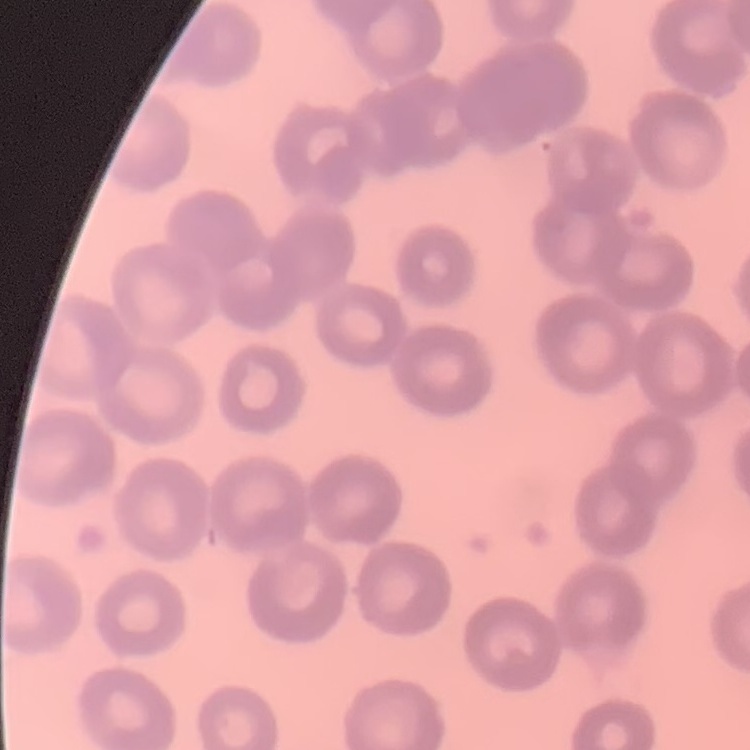
Summary:
  - Erythrocyte morphology: no rouleaux formation
  - Stain: Field's or Giemsa
  - Preparation: thin blood film
  - Image type: square crop of a larger photomicrograph